Outline each blood parasite and name the species.
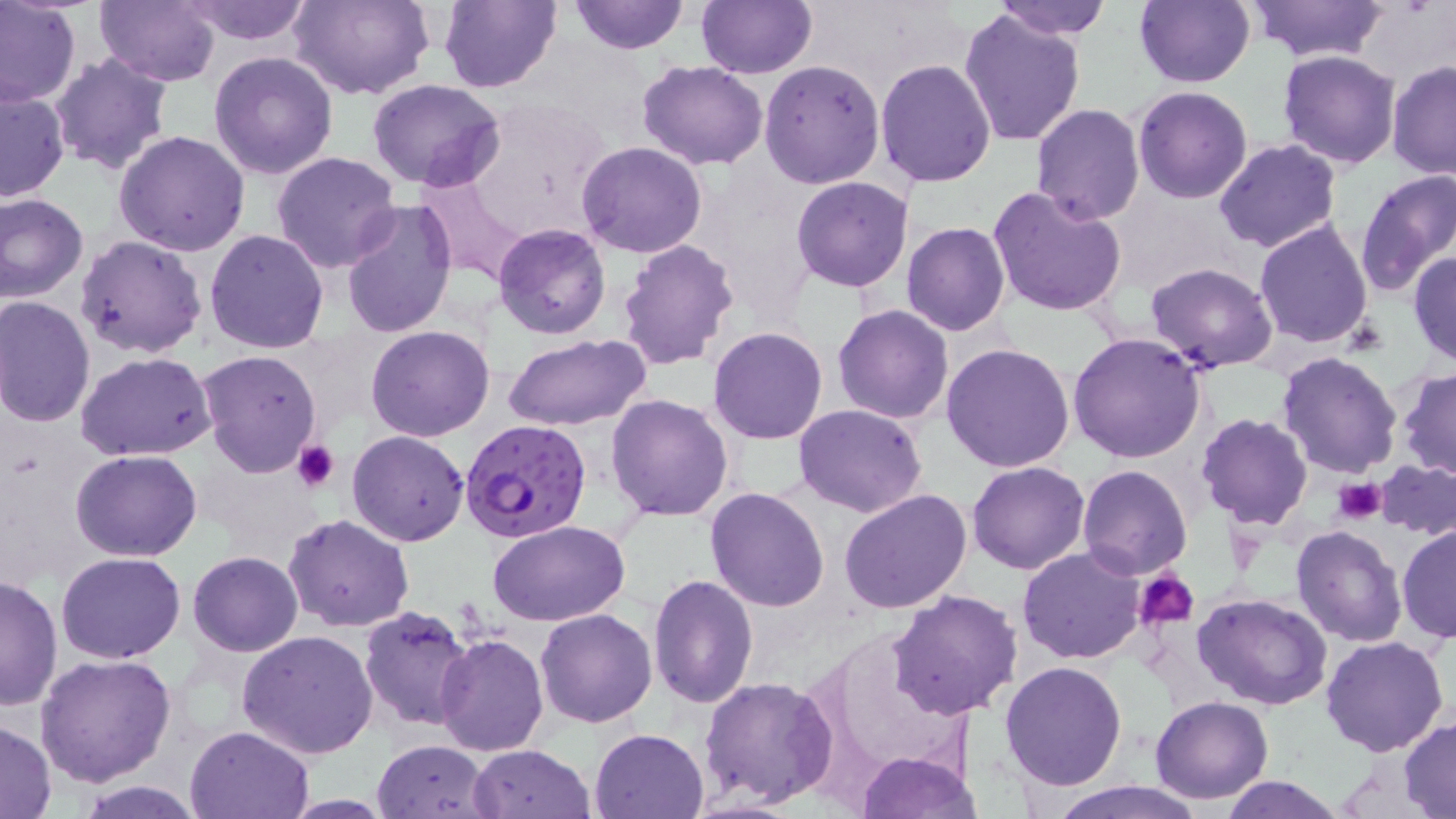
Approximate bounding boxes as named x1/y1/x2/y2 corners in pixels.
Plasmodium falciparum-infected red blood cells: (x1=461, y1=418, x2=594, y2=543).
No Plasmodium ovale, Plasmodium malariae, Plasmodium vivax, Babesia divergens, or Trypanosoma brucei observed.

Platelet locations: (x1=291, y1=440, x2=338, y2=493), (x1=1334, y1=477, x2=1387, y2=524), (x1=1133, y1=568, x2=1200, y2=630). Uninfected red blood cell locations: (x1=0, y1=0, x2=81, y2=107), (x1=95, y1=0, x2=221, y2=85), (x1=182, y1=0, x2=314, y2=45), (x1=289, y1=0, x2=434, y2=101), (x1=439, y1=0, x2=562, y2=93), (x1=569, y1=0, x2=690, y2=55), (x1=697, y1=0, x2=816, y2=79), (x1=992, y1=0, x2=1112, y2=41), (x1=1134, y1=0, x2=1254, y2=88), (x1=1243, y1=0, x2=1389, y2=62), (x1=684, y1=1, x2=803, y2=148), (x1=958, y1=7, x2=1086, y2=146), (x1=49, y1=49, x2=175, y2=175), (x1=1278, y1=50, x2=1400, y2=169), (x1=209, y1=53, x2=338, y2=179), (x1=876, y1=59, x2=997, y2=187), (x1=637, y1=60, x2=768, y2=168), (x1=759, y1=60, x2=886, y2=190), (x1=1387, y1=60, x2=1456, y2=180), (x1=365, y1=77, x2=507, y2=191), (x1=1133, y1=86, x2=1253, y2=203), (x1=0, y1=87, x2=71, y2=201), (x1=1030, y1=104, x2=1144, y2=224), (x1=114, y1=130, x2=250, y2=257), (x1=1212, y1=139, x2=1342, y2=253), (x1=577, y1=141, x2=708, y2=257), (x1=271, y1=152, x2=401, y2=274), (x1=1355, y1=170, x2=1456, y2=296), (x1=790, y1=176, x2=912, y2=291), (x1=989, y1=185, x2=1130, y2=318), (x1=1, y1=193, x2=90, y2=306), (x1=340, y1=199, x2=456, y2=340), (x1=1254, y1=219, x2=1374, y2=351), (x1=902, y1=222, x2=1009, y2=335), (x1=494, y1=223, x2=610, y2=339), (x1=206, y1=228, x2=328, y2=354), (x1=75, y1=234, x2=208, y2=358), (x1=617, y1=238, x2=740, y2=370), (x1=1408, y1=251, x2=1456, y2=366), (x1=1145, y1=261, x2=1278, y2=372), (x1=0, y1=295, x2=97, y2=428), (x1=833, y1=304, x2=954, y2=424), (x1=366, y1=326, x2=494, y2=442), (x1=709, y1=328, x2=828, y2=444), (x1=1067, y1=332, x2=1208, y2=464), (x1=503, y1=334, x2=651, y2=432), (x1=941, y1=342, x2=1075, y2=473), (x1=197, y1=349, x2=322, y2=477), (x1=75, y1=351, x2=217, y2=461), (x1=1277, y1=351, x2=1404, y2=479), (x1=1397, y1=368, x2=1456, y2=480), (x1=606, y1=394, x2=732, y2=522), (x1=793, y1=403, x2=927, y2=518), (x1=1195, y1=413, x2=1312, y2=530), (x1=347, y1=430, x2=470, y2=547), (x1=71, y1=450, x2=203, y2=562), (x1=1373, y1=458, x2=1456, y2=540), (x1=967, y1=461, x2=1090, y2=574), (x1=1078, y1=466, x2=1193, y2=580), (x1=1038, y1=475, x2=1173, y2=625), (x1=705, y1=486, x2=832, y2=611), (x1=838, y1=488, x2=971, y2=613), (x1=283, y1=513, x2=416, y2=632), (x1=486, y1=520, x2=630, y2=626), (x1=1396, y1=524, x2=1455, y2=644), (x1=1292, y1=525, x2=1408, y2=647), (x1=1017, y1=547, x2=1147, y2=663), (x1=56, y1=551, x2=185, y2=662), (x1=187, y1=551, x2=303, y2=656), (x1=0, y1=573, x2=63, y2=712), (x1=648, y1=574, x2=758, y2=707), (x1=888, y1=590, x2=1023, y2=721), (x1=1193, y1=592, x2=1333, y2=711), (x1=359, y1=604, x2=476, y2=731), (x1=534, y1=608, x2=658, y2=728), (x1=236, y1=630, x2=379, y2=758), (x1=434, y1=632, x2=550, y2=755), (x1=1320, y1=635, x2=1450, y2=756), (x1=35, y1=654, x2=176, y2=788), (x1=1000, y1=661, x2=1128, y2=791), (x1=700, y1=676, x2=841, y2=809), (x1=1149, y1=695, x2=1274, y2=803), (x1=1400, y1=718, x2=1456, y2=816), (x1=0, y1=719, x2=55, y2=819), (x1=185, y1=724, x2=315, y2=817), (x1=589, y1=727, x2=710, y2=818), (x1=373, y1=739, x2=496, y2=817), (x1=469, y1=744, x2=595, y2=819), (x1=858, y1=750, x2=981, y2=819), (x1=1220, y1=776, x2=1347, y2=818), (x1=1040, y1=777, x2=1207, y2=818), (x1=79, y1=781, x2=203, y2=817). Slide-level diagnosis: Plasmodium falciparum. Captured at 1000x magnification. Image is 1456×819 pixels. Thin blood smear. Optical microscopy. May-Grünwald-Giemsa stain. One field of a larger specimen.